Assess the morphology of the erythrocytes.
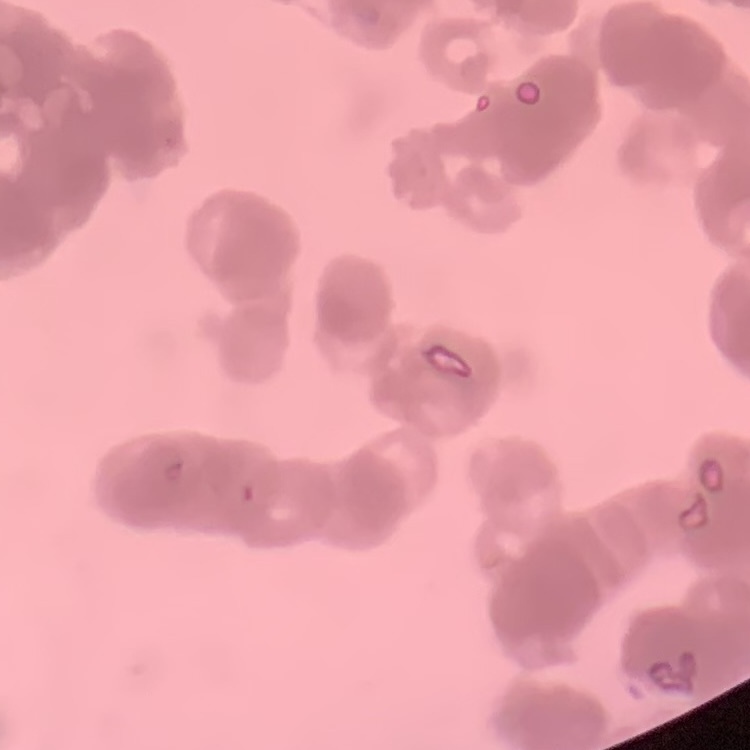
They show rouleaux formation.

Thin peripheral smear. One tile cut from a larger photomicrograph. Stained with either Field's or Giemsa.